Comment on the morphology of the red blood cells.
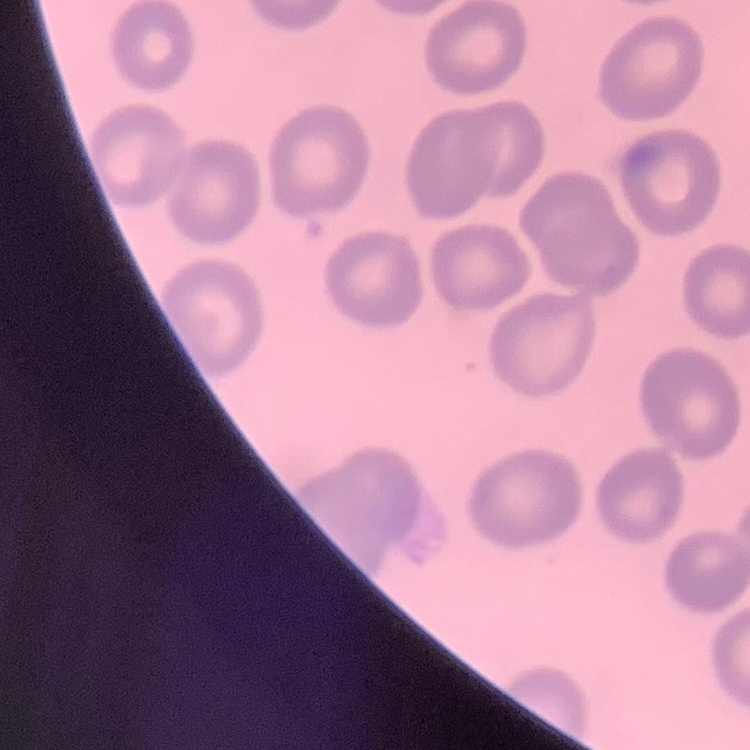

No rouleaux formation.

{
  "image_type": "square crop of a larger photomicrograph",
  "preparation": "thin peripheral smear",
  "stain": "Field's or Giemsa"
}